Give the position of every Plasmodium parasite visible.
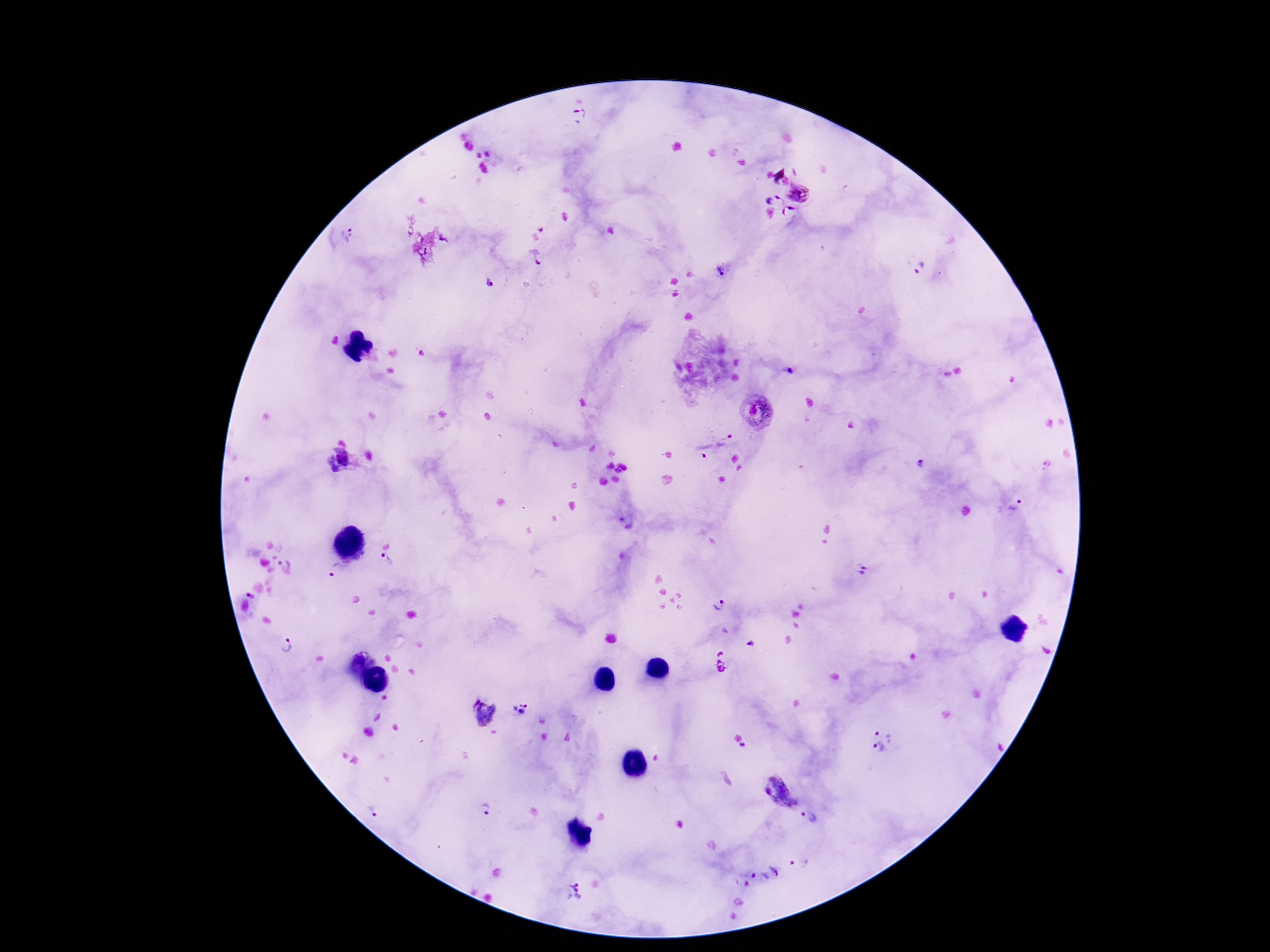

Approximate centers as (x, y) in pixels.
Plasmodium parasites: (579, 116), (799, 193), (773, 201), (790, 213), (349, 233), (538, 258), (920, 267), (721, 273), (489, 285), (792, 372), (757, 413), (727, 441), (702, 450), (338, 460), (919, 464), (1017, 505), (284, 559), (386, 562), (332, 570), (862, 571), (251, 596), (719, 607), (283, 645), (747, 645), (721, 663), (519, 709), (485, 712), (882, 739), (780, 793), (487, 809), (374, 813), (809, 817), (799, 862), (763, 873), (573, 891).

Summary:
  - Patient malaria status: infected
  - Magnification: 100x
  - Field of view: one from this slide
  - Capture: smartphone camera through the microscope eyepiece
  - Stain: Giemsa
  - Image size: 1270×952 pixels
  - Preparation: thick blood smear